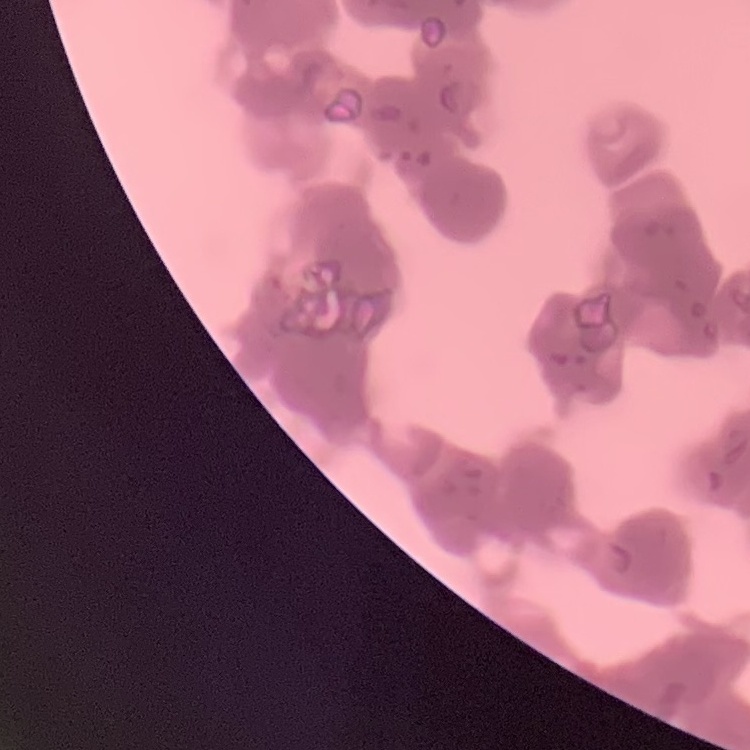

Summary:
  - Red blood cell morphology: rouleaux formation
  - Preparation: thin blood film
  - Image type: square crop of a larger photomicrograph
  - Stain: Field's or Giemsa